Report the malaria status of this cell.
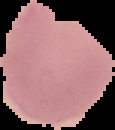

Parasitized.

The area outside the segmented cell region is set to black. Image is 115×130 pixels. From a thin blood smear.